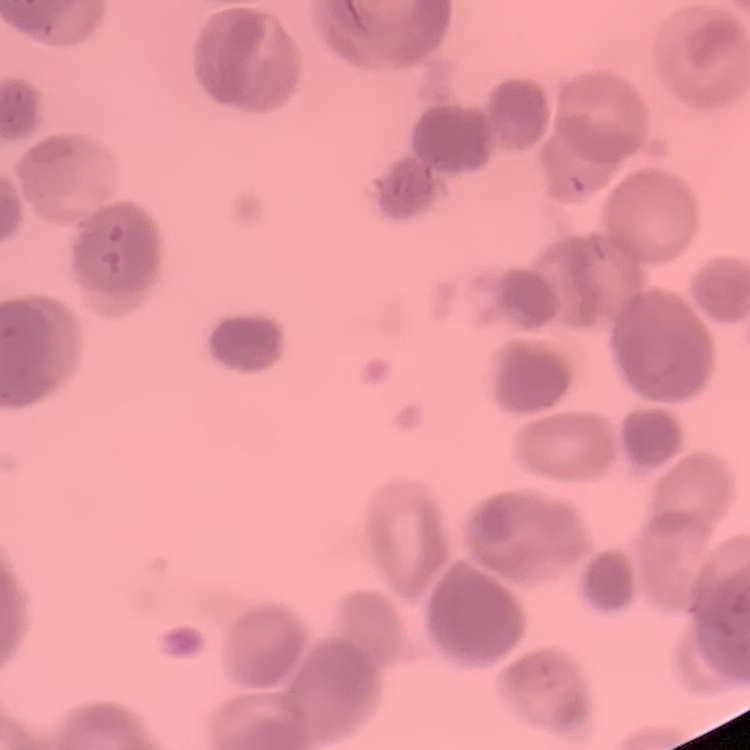
The erythrocytes exhibit rouleaux formation. Thin blood film. One tile cut from a larger photomicrograph. Field's or Giemsa stain.